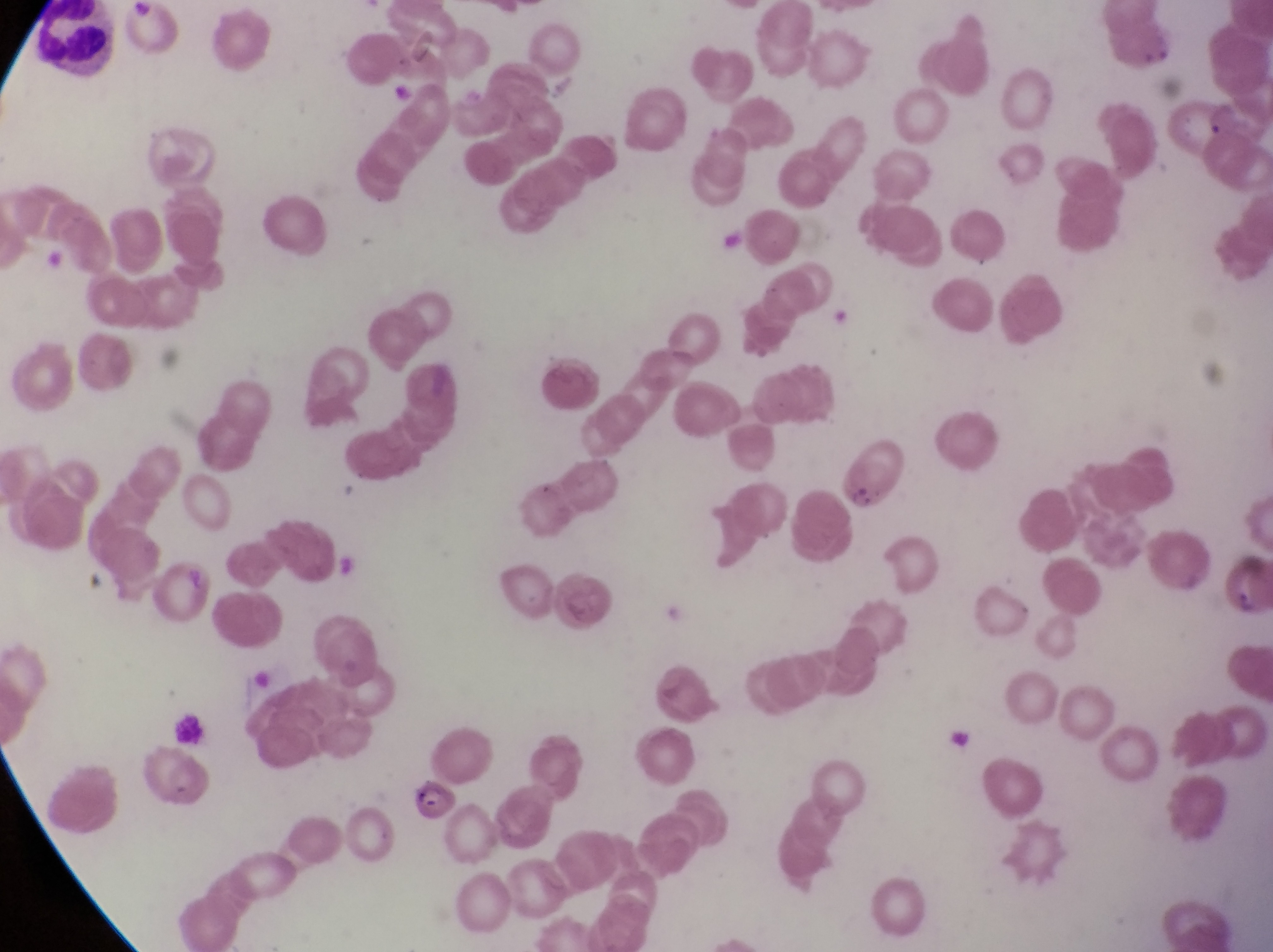
capture: smartphone photograph through the eyepiece of an Olympus CX-23 microscope
parasitised_red_blood_cell_locations: 'approximate bounding boxes as {left, top, right, bottom} in pixels: {831, 434, 911, 514}, {412, 776, 457, 823}'
leukocyte_locations: 'approximate bounding boxes as {left, top, right, bottom} in pixels: {32, 1, 127, 74}, {173, 712, 211, 749}'
image_size: 1273×952 pixels
magnification: 1000x
country: Uganda
preparation: thin blood smear
field_of_view: single